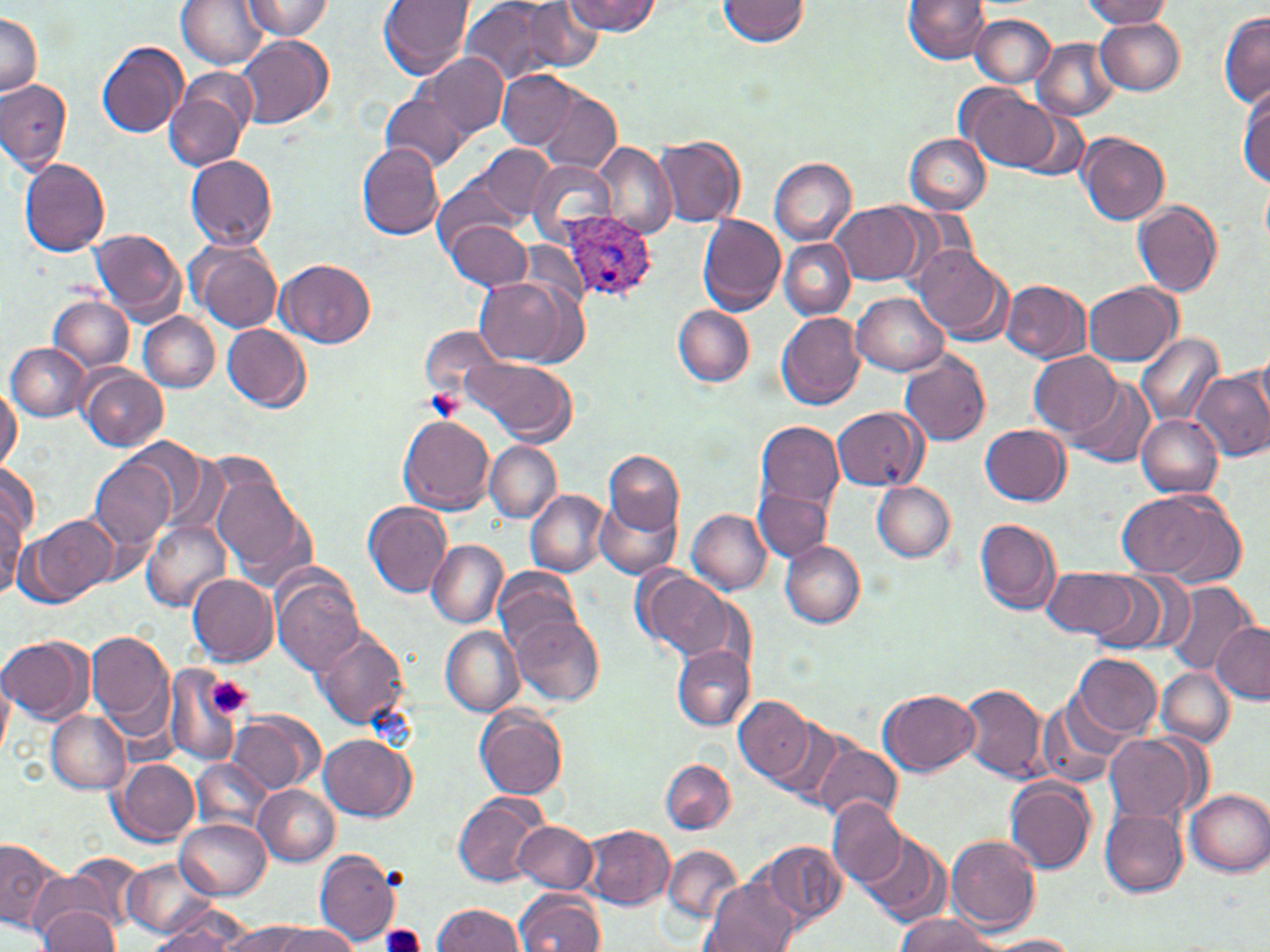
Approximate bounding boxes as (x1, y1, x2, y2) in pixels. Plasmodium ovale-infected red blood cell locations: (563, 213, 658, 303). Uninfected red blood cell locations: (176, 0, 268, 69), (242, 0, 335, 39), (377, 0, 474, 79), (459, 0, 559, 88), (564, 0, 660, 36), (718, 0, 810, 45), (902, 0, 988, 64), (1081, 0, 1173, 27), (516, 2, 602, 74), (1, 11, 40, 98), (1218, 11, 1270, 108), (971, 14, 1054, 87), (1094, 16, 1186, 93), (236, 35, 333, 130), (1033, 38, 1119, 121), (96, 41, 187, 139), (412, 53, 507, 144), (165, 68, 256, 172), (498, 69, 580, 149), (0, 78, 72, 173), (960, 85, 1062, 173), (537, 87, 622, 173), (1238, 87, 1270, 186), (378, 91, 469, 175), (1076, 131, 1169, 226), (906, 134, 989, 213), (655, 136, 745, 227), (474, 143, 556, 223), (593, 143, 675, 240), (357, 144, 444, 239), (185, 155, 278, 250), (770, 157, 856, 244), (19, 158, 111, 257), (526, 159, 616, 244), (434, 175, 520, 254), (1261, 177, 1270, 253), (1133, 201, 1224, 297), (832, 202, 926, 284), (697, 214, 785, 314), (445, 219, 531, 291), (90, 227, 186, 323), (779, 239, 854, 319), (189, 240, 282, 332), (913, 246, 1011, 342), (276, 258, 376, 349), (474, 276, 578, 366), (1002, 279, 1091, 363), (1084, 283, 1181, 365), (852, 291, 950, 374), (51, 295, 132, 372), (673, 305, 754, 386), (776, 311, 866, 410), (140, 312, 219, 392), (222, 323, 312, 414), (420, 326, 503, 403), (1137, 332, 1224, 427), (8, 343, 89, 421), (1029, 350, 1122, 437), (1254, 350, 1270, 433), (899, 351, 991, 449), (465, 356, 576, 444), (79, 366, 167, 451), (1191, 366, 1270, 463), (1068, 376, 1156, 467), (0, 382, 20, 475), (831, 406, 926, 490), (1136, 414, 1223, 497), (398, 416, 495, 514), (754, 420, 843, 513), (981, 424, 1070, 505), (120, 439, 215, 529), (484, 442, 560, 523), (605, 451, 683, 533), (89, 453, 178, 553), (0, 464, 39, 547), (211, 477, 309, 577), (871, 480, 955, 561), (1115, 487, 1244, 585), (756, 488, 832, 562), (525, 490, 607, 576), (595, 495, 683, 581), (0, 496, 23, 598), (364, 501, 452, 598), (687, 509, 770, 594), (22, 513, 116, 606), (975, 518, 1062, 616), (141, 521, 229, 611), (427, 539, 506, 627), (781, 539, 864, 628), (635, 566, 736, 665), (1042, 566, 1144, 641), (493, 568, 581, 654), (1076, 569, 1182, 652), (187, 574, 277, 665), (270, 574, 365, 677), (1164, 582, 1259, 676), (513, 615, 604, 705), (1210, 621, 1270, 701), (440, 625, 524, 717), (86, 628, 175, 736), (313, 629, 408, 730), (0, 635, 91, 723), (671, 644, 752, 731), (1072, 652, 1162, 737), (162, 666, 252, 767), (1157, 668, 1233, 748), (0, 673, 13, 761), (959, 683, 1049, 782), (879, 691, 980, 777), (734, 695, 814, 785), (1039, 696, 1125, 788), (474, 707, 568, 800), (47, 710, 129, 793), (226, 710, 321, 793), (764, 714, 846, 805), (1103, 733, 1197, 825), (319, 734, 415, 821), (811, 739, 901, 827), (191, 757, 272, 836), (113, 758, 199, 842), (659, 759, 735, 834), (1004, 776, 1097, 874), (253, 784, 339, 865), (1184, 788, 1270, 877), (452, 794, 546, 887), (828, 800, 907, 890), (1100, 807, 1189, 897), (177, 819, 270, 900), (512, 820, 597, 893), (582, 824, 675, 909), (864, 832, 949, 924), (947, 833, 1041, 932), (0, 835, 67, 932), (759, 840, 846, 929), (662, 844, 745, 926), (314, 848, 399, 947), (67, 854, 147, 931), (123, 856, 214, 939), (27, 870, 128, 949), (705, 880, 796, 952), (516, 889, 605, 952), (151, 904, 251, 951), (434, 904, 525, 951), (37, 906, 120, 951), (895, 913, 1000, 951), (219, 921, 318, 952), (268, 925, 360, 951), (142, 928, 237, 951), (982, 934, 1081, 952). Platelet locations: (208, 678, 253, 718), (381, 923, 426, 952). Slide-level diagnosis: Plasmodium ovale. 1000x magnification. Image is 1270×952 pixels. Optical microscopy. Thin blood film. Single field of view. May-Grünwald-Giemsa stain.